Assess this cell for malaria.
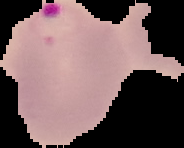
It is parasitized.

From a thin blood film. Image is 184×148 pixels. The area outside the segmented cell region is set to black.